Give the extent of all uninfected red blood cells.
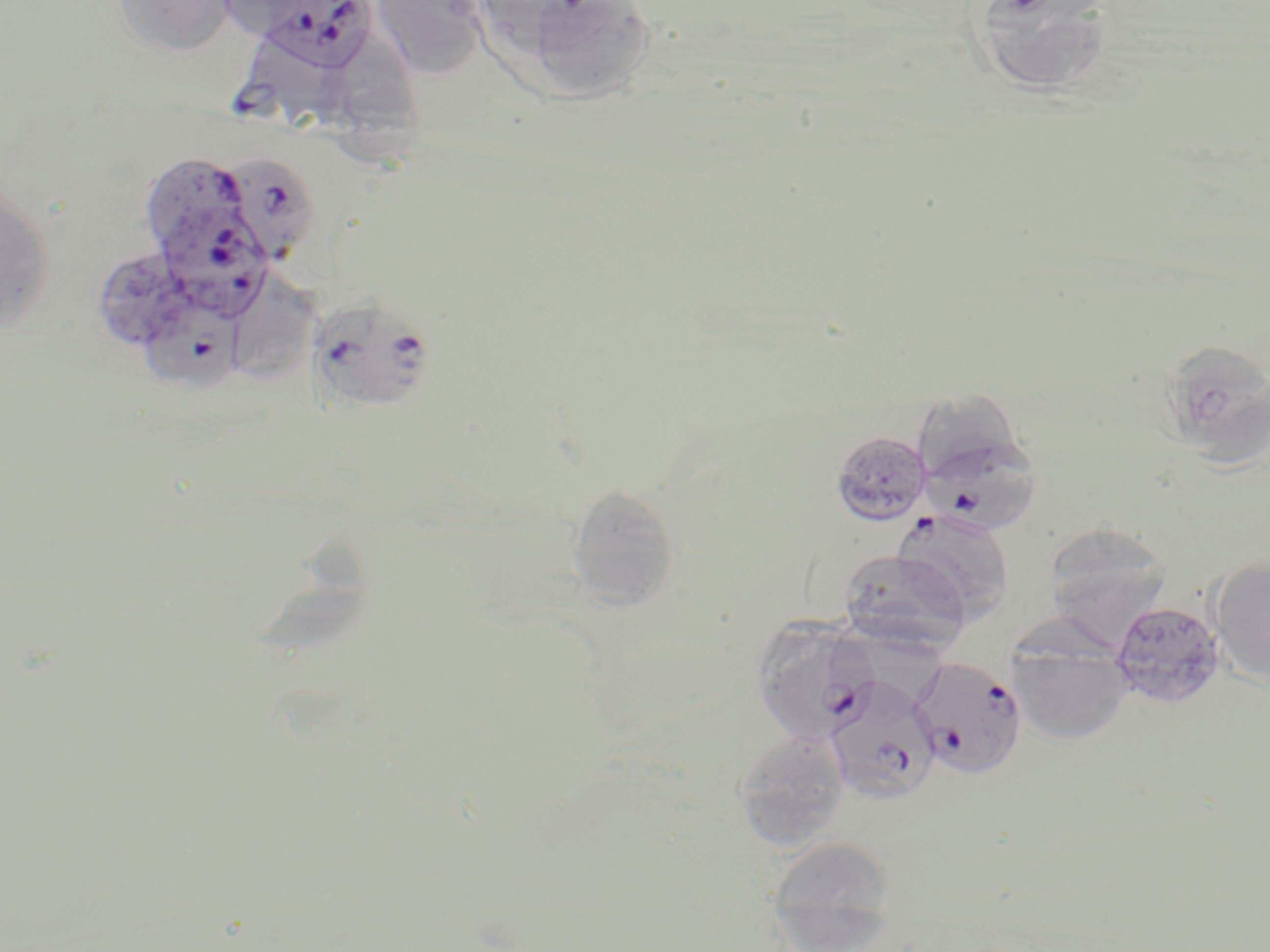

Approximate bounding boxes as (x1, y1, x2, y2) in pixels.
Uninfected red blood cells: (112, 0, 238, 57), (213, 0, 330, 39), (370, 0, 489, 79), (522, 0, 657, 101), (974, 1, 1115, 98), (327, 36, 427, 180), (0, 183, 56, 334), (230, 276, 321, 378), (1168, 343, 1270, 477), (916, 388, 1028, 478), (830, 431, 932, 526), (566, 484, 681, 609), (890, 509, 1016, 621), (1044, 522, 1173, 638), (258, 535, 373, 660), (837, 548, 972, 653), (1208, 558, 1270, 687), (828, 598, 943, 713), (1108, 600, 1226, 709), (1008, 640, 1133, 745), (733, 728, 851, 850), (766, 835, 898, 950).

{
  "slide_level_diagnosis": "Plasmodium falciparum",
  "field_of_view": "one of a larger specimen",
  "preparation": "thin blood smear",
  "plasmodium_falciparum_infected_red_blood_cell_locations": "approximate bounding boxes as (x1, y1, x2, y2) in pixels: (256, 0, 379, 73), (234, 37, 340, 140), (139, 150, 264, 250), (221, 151, 321, 265), (160, 210, 268, 320), (140, 294, 246, 392), (308, 297, 436, 413), (918, 425, 1044, 536), (752, 618, 880, 744), (909, 656, 1027, 778), (824, 673, 941, 806)",
  "image_size": "1270×952 pixels",
  "stain": "May-Grünwald-Giemsa",
  "modality": "optical microscopy",
  "magnification": "1000x"
}